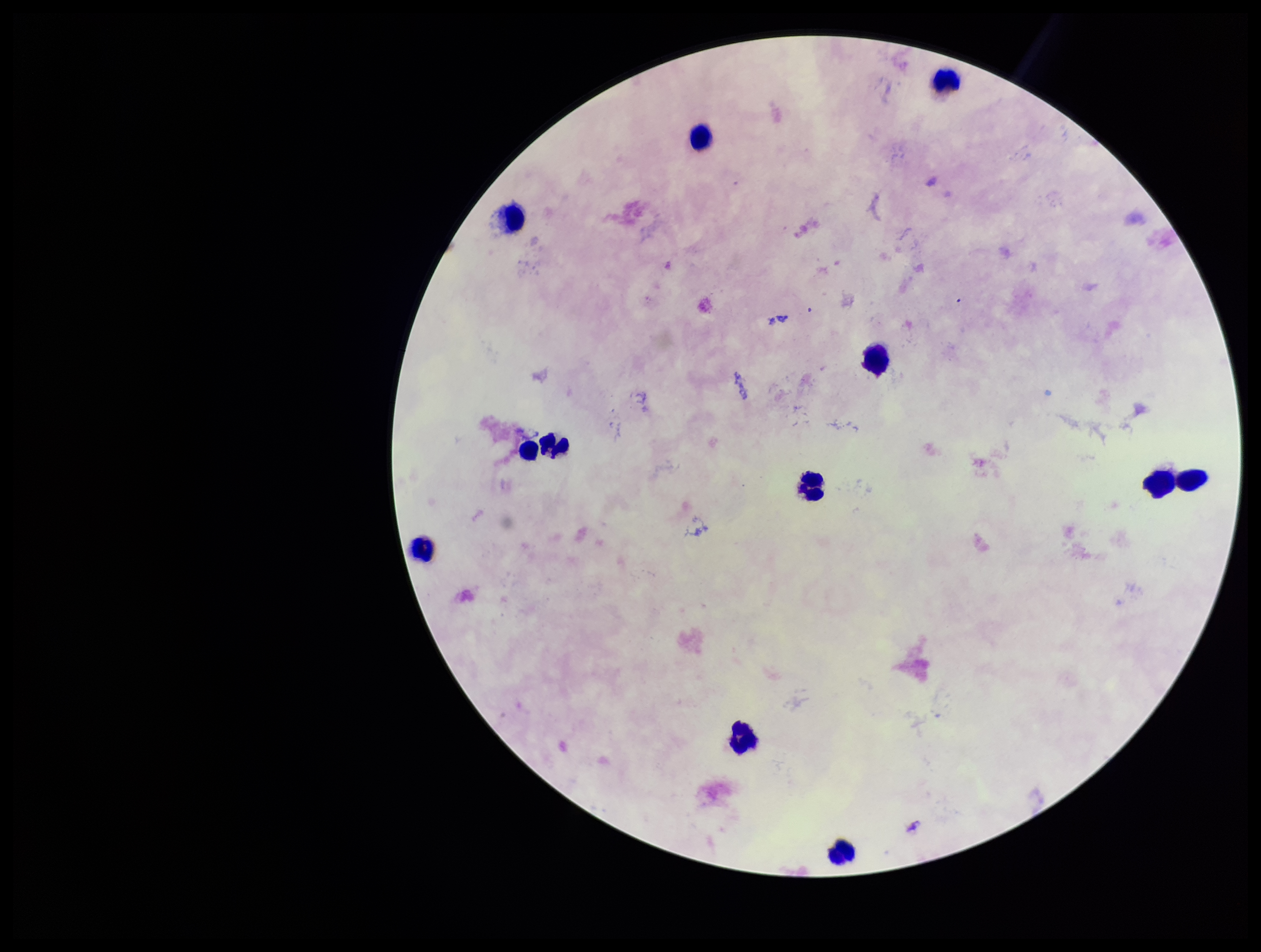
Summary:
  - Capture: smartphone photograph through the microscope eyepiece
  - Image size: 1261×952 pixels
  - Parasite count: 0
  - Preparation: thick blood smear
  - Stain: Giemsa
  - Plasmodium parasites: none identified
  - Patient malaria status: negative
  - Leukocyte count: 12
  - Field of view: one from this slide